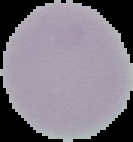
image size = 133×142 pixels
image type = segmented cell region with the area outside set to black
preparation = thin blood film
result = no malaria parasites detected